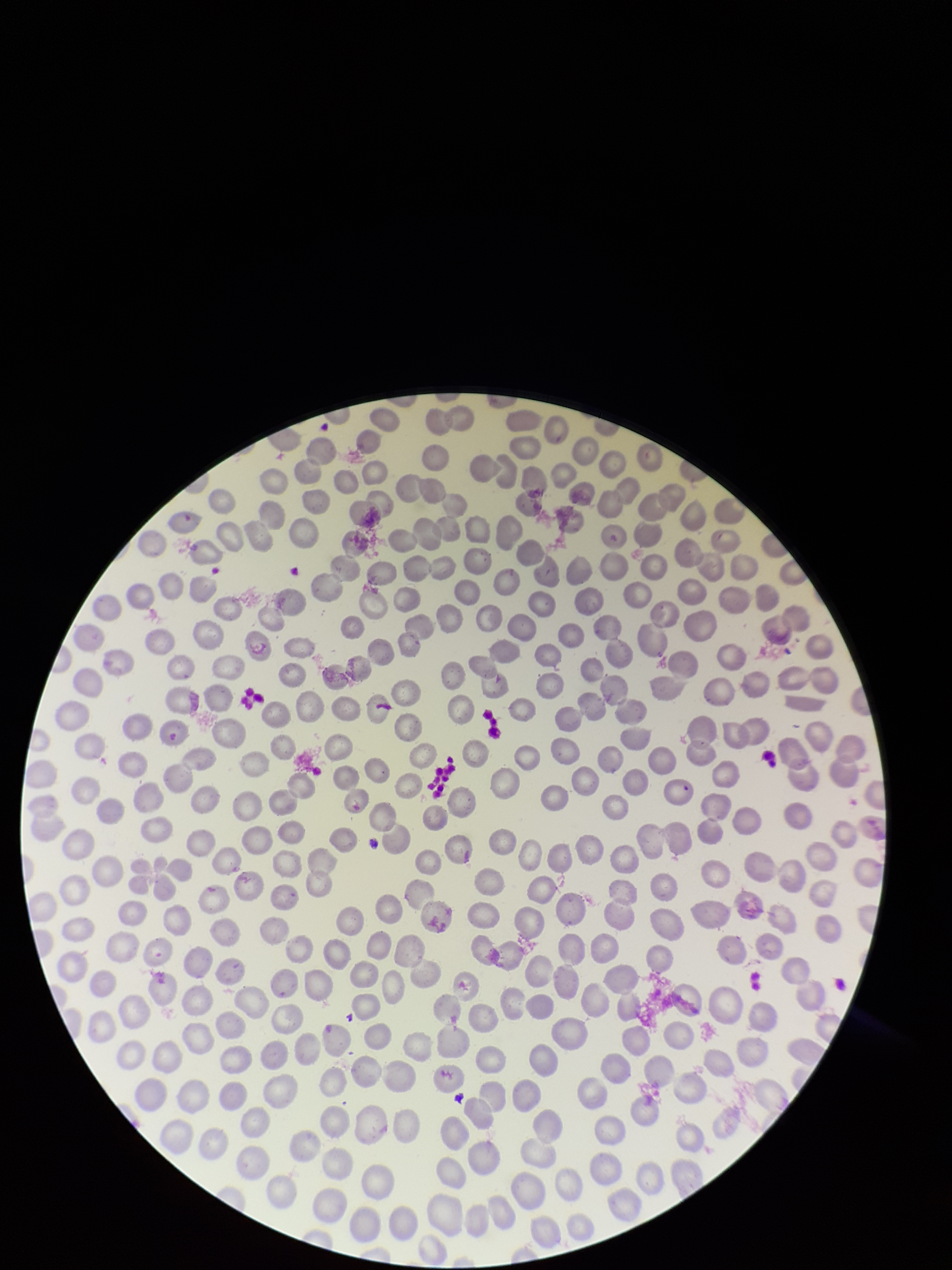
Summary:
  - Image size: 952×1270 pixels
  - Field of view: single
  - Parasitized red blood cells: none identified
  - Patient malaria status: negative
  - Red blood cell count: 291
  - Capture: smartphone photograph through the microscope eyepiece
  - Parasitized red blood cell count: 0
  - Preparation: thin smear
  - Stain: Giemsa